Assess this cell for malaria.
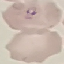

It is parasitized.

image type = automatically extracted cell patch, resized to 64 × 64 pixels
stain = Giemsa
preparation = thin smear
capture = smartphone through the microscope eyepiece